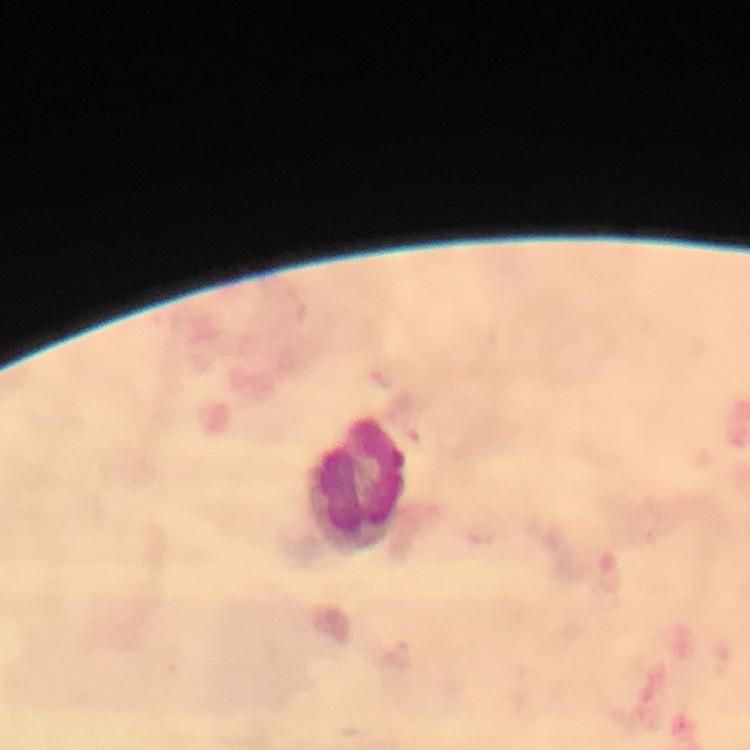
Approximate centers as {x, y} in pixels.
Summary:
  - Leukocyte locations: {357, 481}
  - Cropped from: a single field of view
  - Context: from a diagnostic examination for malaria
  - Plasmodium parasites: none detected
  - Capture: smartphone mounted on the microscope
  - Image size: 750×750 pixels
  - Magnification: 100x
  - Immersion oil: applied
  - Stain: Giemsa
  - Preparation: thick blood smear